Give the preparation type.
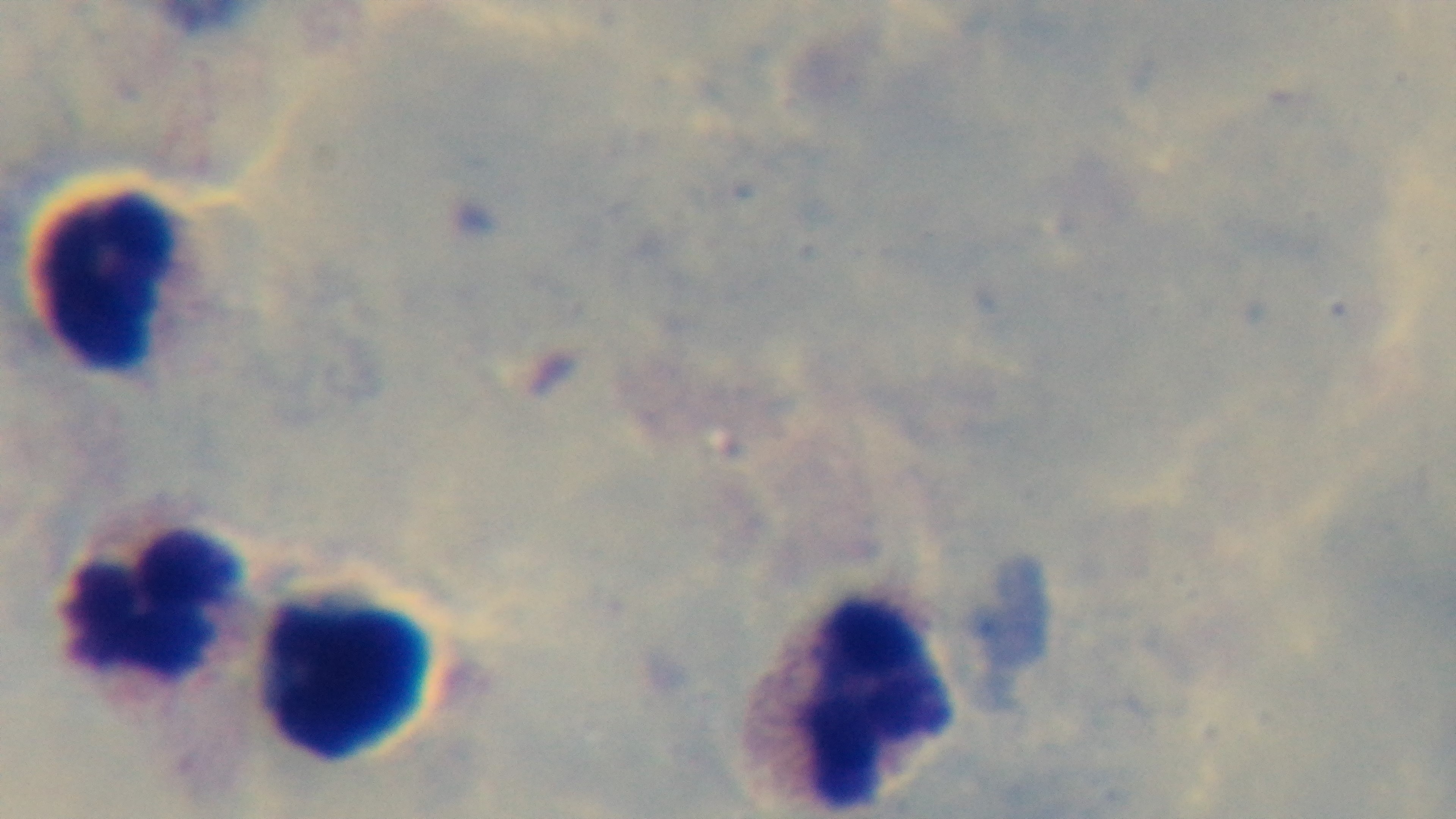

Thick.

Mounted 4K digital camera. One field from the slide. Giemsa-stained. Oil-immersion objective, 100x. Malaria status: negative. Light microscopy.